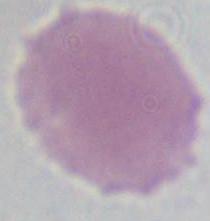

1000x magnification. A red blood cell is shown. Photomicrograph.